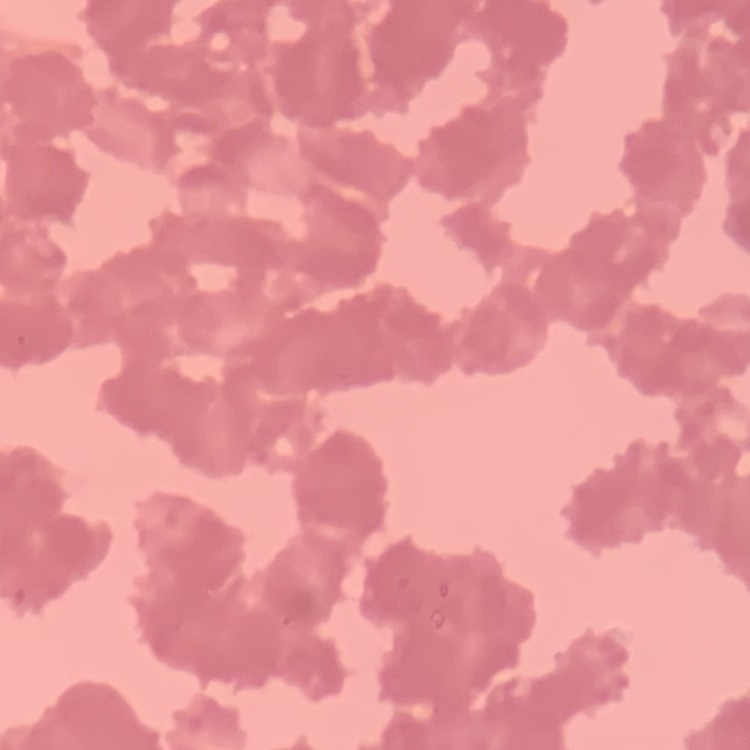 The red blood cells show rouleaux formation. One tile cut from a larger photomicrograph. Stained with either Field's or Giemsa. Thin peripheral smear.